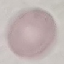

Malaria status: uninfected. Acquired by smartphone through the microscope eyepiece. Thin blood smear. Cell patch, automatically extracted from a larger field of view and resized to 64 × 64 pixels. Giemsa stain.